Identify the preparation type.
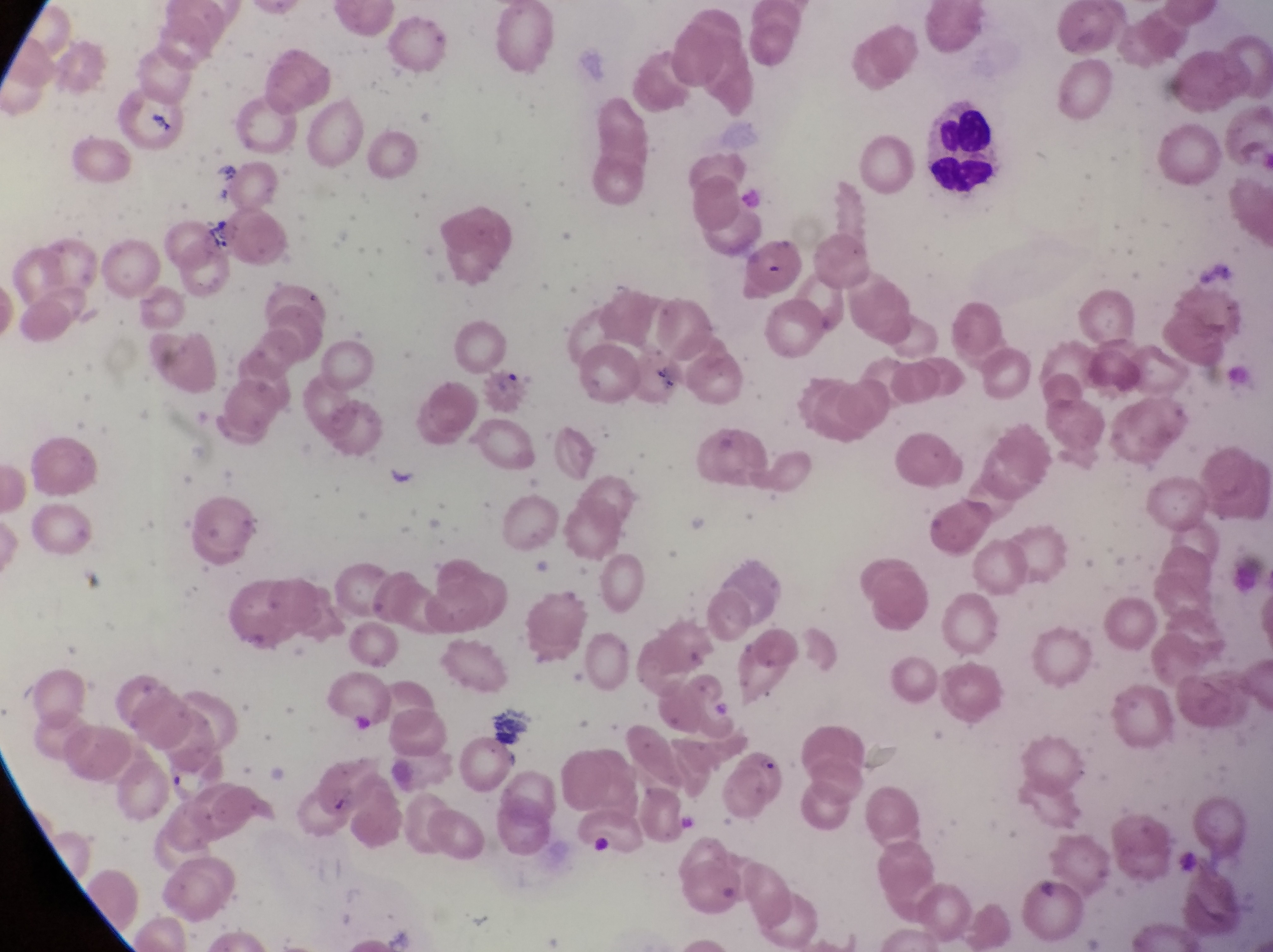
Thin blood film.

Approximate bounding boxes as left top right bottom in pixels. Leukocyte locations: 919 98 1018 208. Parasitised red blood cell locations: 719 751 796 825. Artifact (platelet-like body, stain precipitate, or debris) locations: 587 824 614 863. Magnification of 1000x. Photographed through the eyepiece of an Olympus CX-23 microscope with a smartphone camera. Sample from Uganda. Image is 1273×952 pixels. Single field of view.